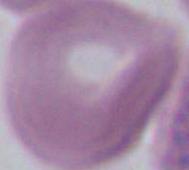 Captured at 1000x magnification. Micrograph. A red blood cell is shown.